Assess for malaria.
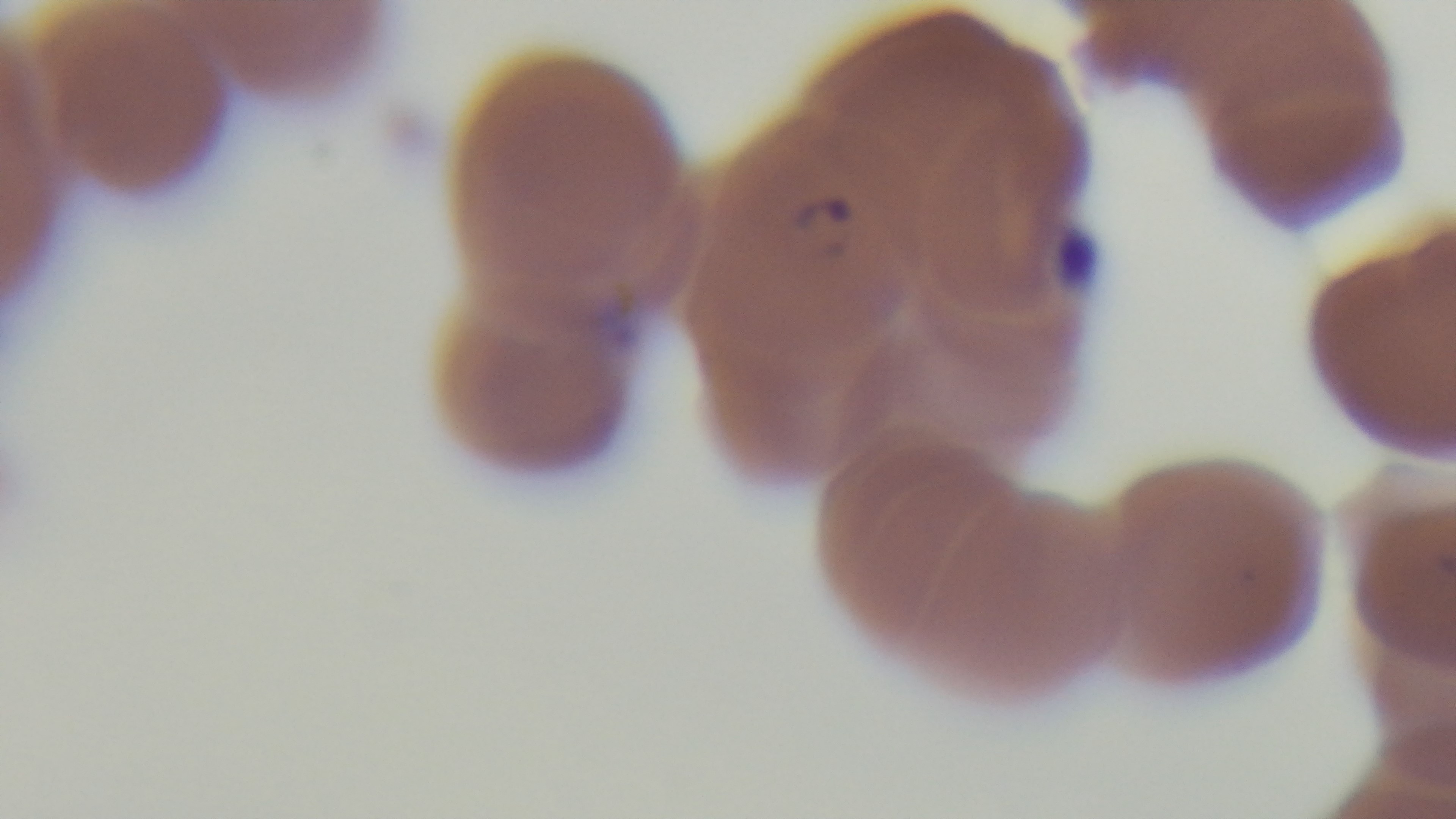

Infected.

modality = light microscopy
objective = 100x oil immersion
stain = Giemsa
capture = mounted 4K digital camera
field of view = single
preparation = thin